Mark where leukocytes are.
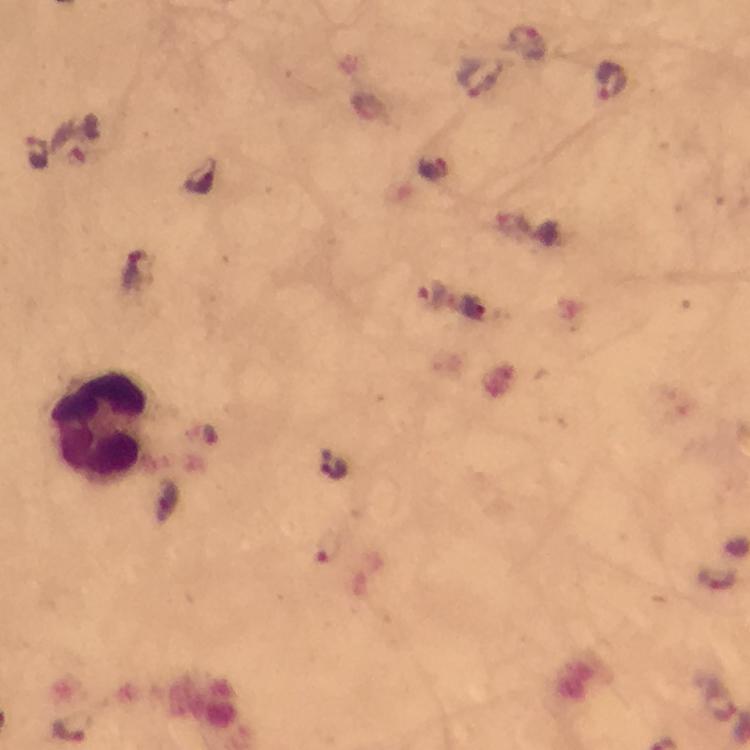

Approximate centers as (x, y) in pixels.
Leukocytes: (100, 425).

Summary:
  - Malaria parasite locations: (525, 44), (476, 79), (611, 79), (431, 297), (717, 579), (70, 727)
  - Preparation: thick blood film
  - Immersion oil: used
  - Magnification: 100x
  - Context: from a diagnostic examination for malaria
  - Image size: 750×750 pixels
  - Cropped from: one field of view
  - Capture: smartphone photograph through a microscope
  - Stain: Giemsa